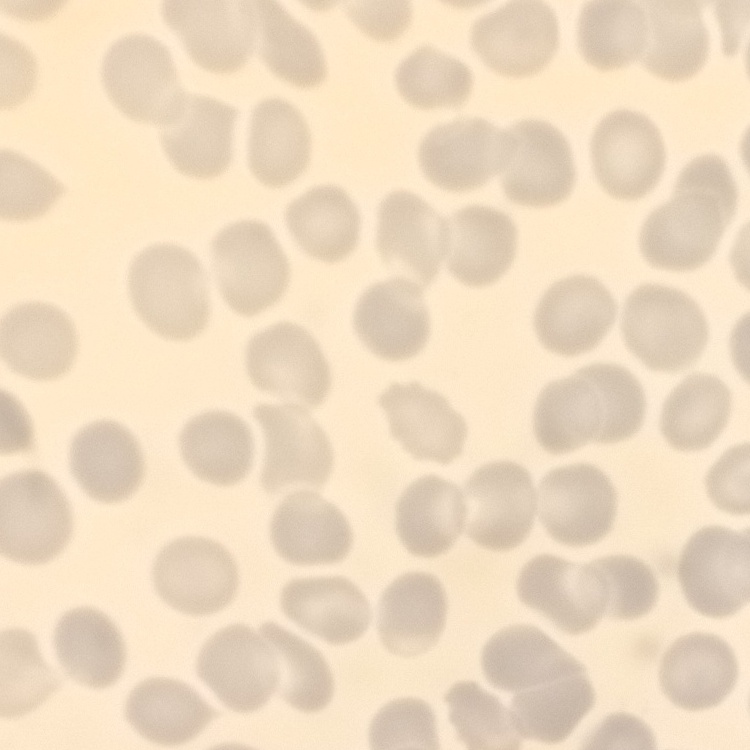

{
  "erythrocyte_morphology": "no rouleaux formation",
  "stain": "Field's or Giemsa",
  "image_type": "square crop of a larger photomicrograph",
  "preparation": "thin blood film"
}